Give the location of every parasitized red blood cell.
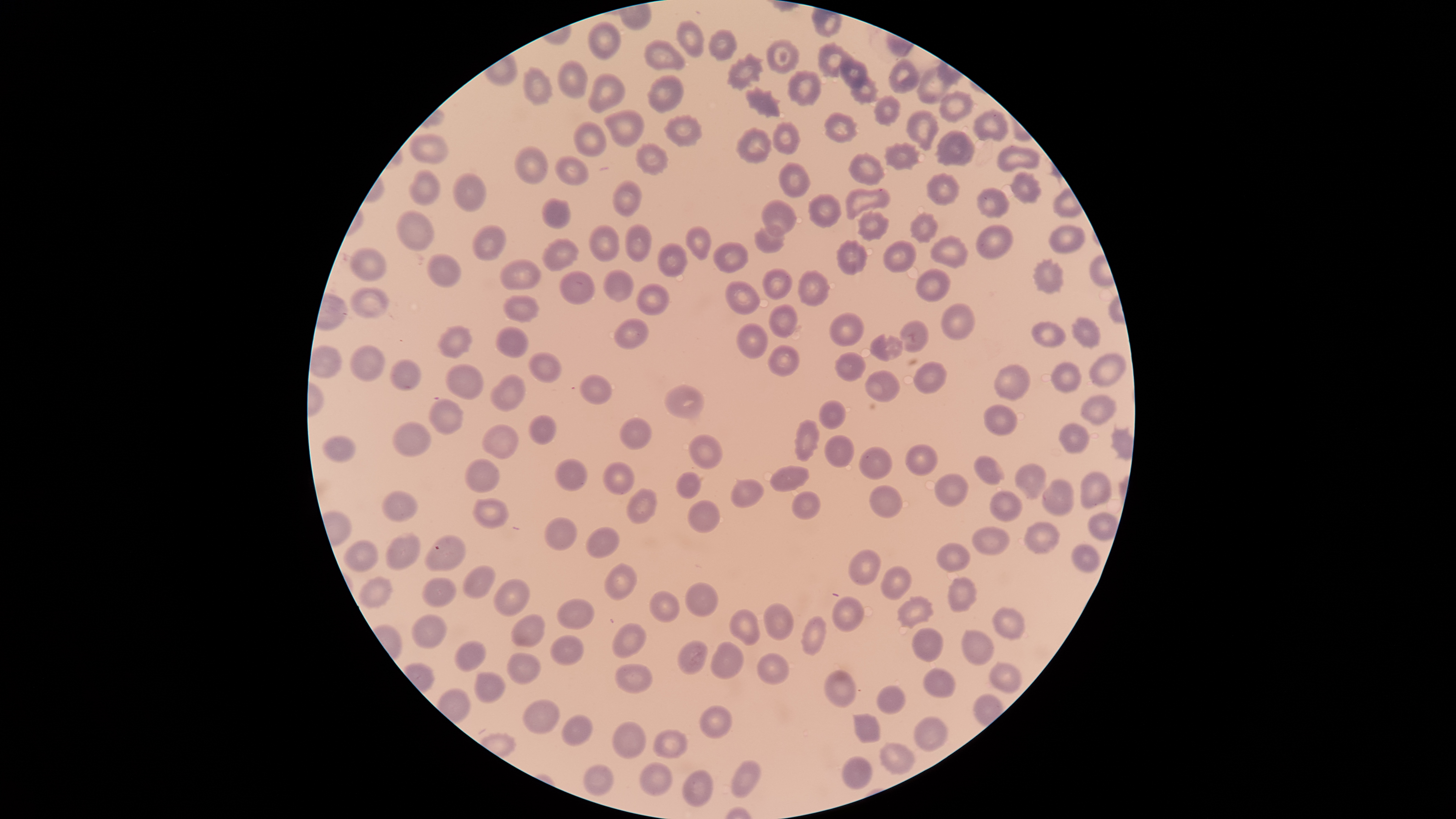

No parasitized red blood cells identified.

Approximate bounding boxes as [left, top, right, bottom] in pixels. Uninfected red blood cells: [587, 20, 621, 61], [675, 20, 705, 57], [708, 28, 737, 62], [644, 38, 685, 71], [767, 38, 799, 74], [816, 42, 851, 78], [725, 52, 764, 91], [888, 57, 920, 95], [556, 59, 589, 100], [839, 60, 868, 88], [787, 68, 822, 107], [916, 68, 948, 105], [588, 73, 624, 113], [646, 74, 684, 114], [850, 77, 879, 105], [744, 86, 782, 118], [938, 91, 976, 122], [873, 95, 902, 126], [972, 108, 1009, 143], [603, 109, 645, 148], [906, 109, 940, 151], [824, 112, 859, 143], [662, 114, 703, 147], [573, 121, 606, 156], [771, 122, 803, 156], [735, 127, 772, 163], [933, 127, 976, 167], [408, 133, 449, 165], [634, 141, 671, 176], [882, 141, 921, 171], [513, 146, 548, 184], [997, 146, 1040, 171], [845, 152, 886, 186], [555, 155, 590, 187], [779, 161, 811, 198], [407, 168, 443, 207], [926, 171, 961, 206], [1010, 171, 1042, 206], [452, 173, 487, 213], [611, 180, 643, 218], [845, 188, 890, 220], [977, 188, 1012, 219], [807, 193, 843, 228], [541, 198, 572, 228], [761, 198, 797, 237], [395, 209, 436, 250], [857, 209, 890, 242], [909, 211, 940, 243], [470, 223, 508, 260], [589, 223, 621, 263], [625, 223, 652, 262], [753, 224, 786, 253], [975, 224, 1014, 260], [1049, 224, 1086, 253], [684, 225, 713, 260], [929, 234, 969, 269], [539, 237, 580, 272], [835, 238, 868, 275], [882, 240, 917, 273], [657, 242, 688, 276], [712, 242, 750, 274], [350, 247, 387, 281], [427, 253, 462, 287], [1030, 257, 1066, 296], [499, 259, 541, 291], [761, 266, 793, 301], [603, 268, 635, 303], [797, 268, 831, 307], [914, 268, 951, 303], [558, 269, 595, 305], [725, 280, 762, 315], [636, 283, 670, 315], [350, 287, 389, 318], [502, 294, 541, 324], [767, 302, 798, 339], [941, 302, 977, 341], [830, 312, 865, 346], [1071, 316, 1101, 350], [613, 317, 649, 350], [898, 320, 929, 353], [1032, 320, 1065, 348], [735, 322, 768, 359], [437, 324, 473, 359], [494, 327, 529, 356], [869, 333, 903, 362], [349, 343, 385, 383], [767, 343, 799, 377], [310, 344, 342, 378], [528, 351, 563, 385], [834, 351, 868, 381], [1088, 353, 1127, 388], [388, 358, 422, 392], [912, 360, 947, 395], [446, 362, 485, 401], [1050, 362, 1082, 393], [993, 364, 1032, 401], [864, 369, 901, 402], [578, 373, 612, 404], [489, 374, 528, 412], [663, 384, 705, 421], [1079, 394, 1115, 426], [428, 398, 464, 435], [818, 399, 847, 430], [982, 404, 1020, 437], [528, 415, 557, 445], [619, 416, 653, 450], [793, 417, 821, 462], [392, 420, 432, 458], [1058, 421, 1089, 455], [482, 424, 519, 461], [688, 433, 724, 470], [822, 435, 855, 469], [321, 436, 356, 463], [905, 443, 939, 478], [858, 445, 893, 481], [973, 455, 1005, 486], [464, 457, 500, 494], [554, 458, 589, 491], [602, 461, 635, 495], [1013, 462, 1047, 500], [769, 464, 810, 493], [1080, 470, 1112, 511], [675, 471, 703, 500], [934, 473, 970, 509], [731, 478, 766, 507], [1040, 478, 1075, 517], [869, 484, 903, 519], [627, 487, 657, 524], [791, 489, 822, 520], [989, 489, 1024, 523], [380, 490, 419, 521], [472, 496, 509, 529], [687, 499, 720, 534], [1087, 510, 1119, 541], [542, 516, 577, 550], [1023, 521, 1061, 555], [585, 526, 620, 559], [972, 527, 1011, 556], [384, 532, 422, 572], [424, 533, 467, 572], [343, 539, 379, 572], [935, 542, 971, 572], [1072, 544, 1101, 572], [847, 548, 882, 586], [604, 562, 638, 602], [880, 564, 913, 601], [462, 565, 496, 600], [357, 576, 394, 611], [947, 576, 979, 612], [420, 577, 458, 608], [493, 578, 530, 618], [684, 581, 719, 617], [648, 589, 681, 623], [896, 595, 934, 630], [832, 596, 863, 633], [556, 598, 596, 630], [763, 602, 795, 642], [992, 606, 1026, 641], [728, 608, 762, 647], [411, 613, 449, 650], [511, 613, 546, 648], [800, 617, 827, 657], [612, 622, 646, 659], [911, 627, 945, 662], [961, 628, 994, 666], [550, 634, 584, 667], [454, 640, 486, 673], [676, 640, 707, 675], [711, 640, 744, 679], [757, 651, 790, 685], [506, 653, 541, 686], [989, 660, 1023, 694], [614, 663, 654, 694], [923, 667, 957, 699], [824, 668, 858, 710], [473, 671, 507, 704], [876, 684, 906, 714], [521, 698, 561, 734], [699, 706, 733, 739], [852, 712, 881, 743], [561, 714, 592, 747], [913, 715, 948, 752], [611, 721, 647, 758], [652, 728, 688, 758], [877, 742, 916, 776], [841, 756, 873, 789], [729, 760, 761, 799], [639, 761, 673, 796], [582, 765, 613, 797], [682, 768, 712, 808]. Single field of view. Image is 1456×819 pixels. Thin blood film. Smartphone photograph through the microscope eyepiece. The visible region is circular. Giemsa stain.